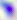
modality = micrograph
identification = Toxoplasma gondii
magnification = 400x